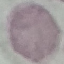
Summary:
  - Malaria status: uninfected
  - Preparation: thin smear
  - Capture: smartphone camera at the microscope eyepiece
  - Image type: automatically extracted cell patch, resized to 64 × 64 pixels
  - Stain: Giemsa